Classify this cell by malaria status.
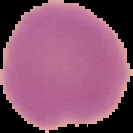

It is uninfected.

image_type: cell region segmented out of the field of view; surrounding area masked to black
preparation: thin blood smear
image_size: 133×133 pixels